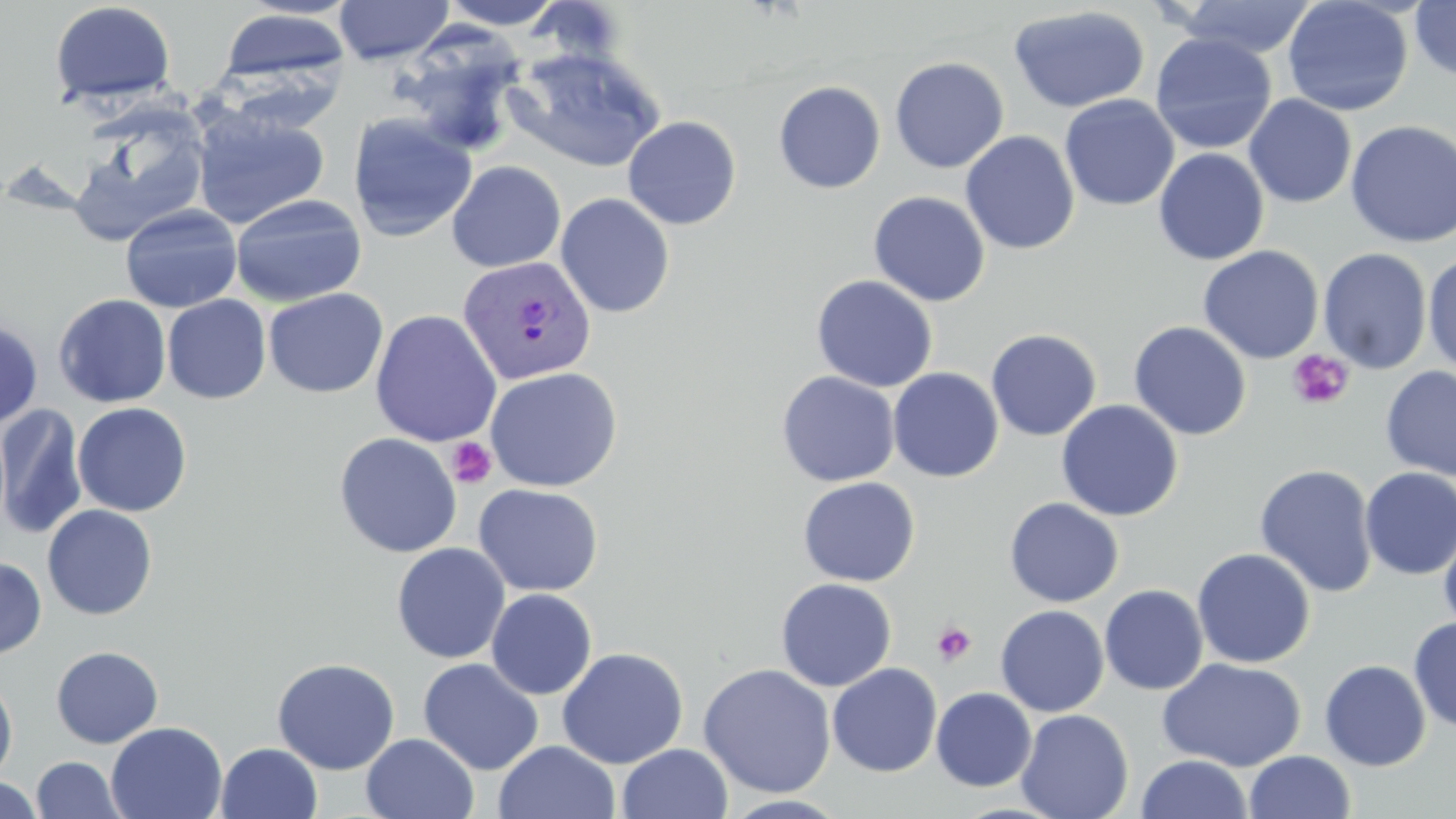

Summary:
  - Coordinate format: approximate bounding boxes as (x1, y1, x2, y2) in pixels
  - Platelet locations: (1287, 349, 1354, 410), (447, 437, 497, 489), (932, 622, 977, 666)
  - Uninfected red blood cell locations: (334, 0, 454, 64), (438, 0, 568, 29), (1282, 0, 1413, 117), (49, 1, 176, 109), (1165, 1, 1320, 59), (1409, 1, 1456, 82), (1009, 6, 1150, 113), (217, 7, 350, 89), (387, 28, 529, 156), (1150, 33, 1277, 154), (503, 47, 667, 173), (889, 56, 1010, 173), (773, 81, 886, 194), (1059, 94, 1180, 211), (1243, 94, 1357, 208), (191, 105, 331, 230), (69, 106, 211, 246), (347, 112, 477, 242), (622, 116, 741, 230), (1345, 119, 1456, 249), (960, 131, 1080, 255), (1153, 148, 1269, 265), (447, 161, 566, 272), (868, 191, 990, 306), (555, 193, 675, 318), (230, 194, 367, 307), (120, 204, 242, 313), (1197, 246, 1324, 364), (1318, 247, 1432, 374), (1423, 252, 1456, 378), (811, 274, 938, 393), (263, 288, 388, 398), (53, 294, 172, 408), (162, 294, 271, 404), (369, 309, 502, 447), (0, 319, 43, 429), (1128, 321, 1252, 441), (986, 329, 1102, 441), (1380, 365, 1456, 482), (484, 366, 623, 492), (888, 367, 1004, 482), (776, 371, 900, 486), (1056, 399, 1183, 521), (72, 402, 192, 517), (0, 405, 88, 540), (333, 432, 463, 558), (1254, 463, 1378, 598), (1359, 467, 1456, 579), (796, 477, 920, 587), (473, 483, 604, 596), (1004, 497, 1124, 607), (41, 504, 158, 619), (1438, 519, 1456, 641), (391, 542, 510, 663), (1192, 548, 1315, 668), (0, 555, 47, 661), (775, 578, 897, 691), (1100, 585, 1208, 695), (485, 588, 598, 699), (995, 605, 1110, 717), (1408, 616, 1456, 732), (51, 645, 164, 748), (557, 647, 689, 769), (272, 657, 400, 774), (1157, 657, 1306, 771), (418, 658, 543, 776), (1319, 660, 1431, 771), (698, 663, 837, 798), (827, 663, 942, 777), (0, 674, 18, 783), (931, 687, 1036, 791), (1015, 709, 1134, 819), (105, 721, 228, 819), (361, 732, 479, 819), (493, 740, 621, 819), (216, 742, 322, 819), (617, 744, 733, 819), (1244, 749, 1356, 819), (1137, 754, 1252, 818), (31, 757, 123, 818), (1, 775, 43, 818), (720, 794, 850, 818)
  - Plasmodium vivax-infected red blood cell locations: (457, 255, 597, 384)
  - Slide-level diagnosis: Plasmodium vivax
  - Magnification: 1000x
  - Preparation: thin blood smear
  - Image size: 1456×819 pixels
  - Modality: light microscopy
  - Field of view: single
  - Stain: May-Grünwald-Giemsa